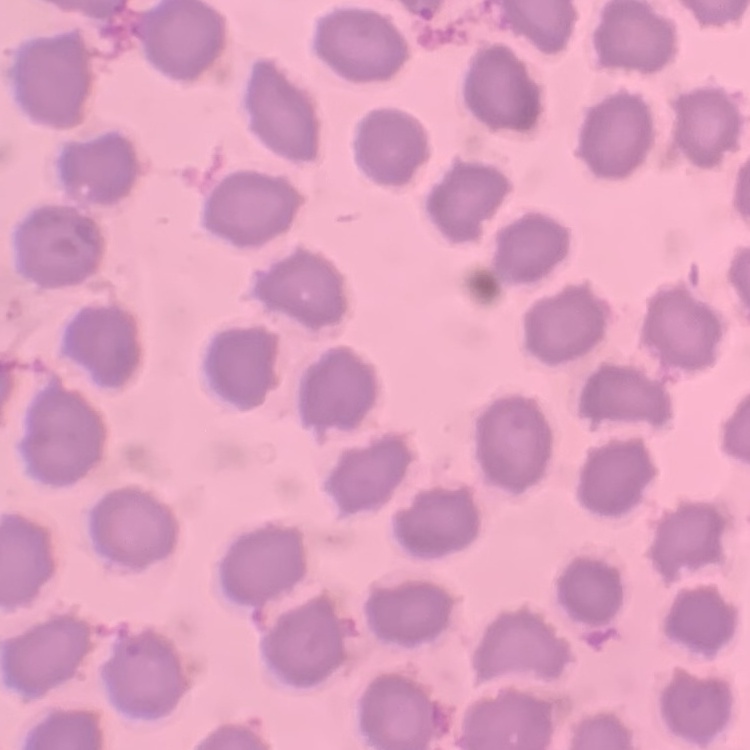
red blood cell morphology = no rouleaux formation
stain = Field's or Giemsa
image type = square crop of a larger photomicrograph
preparation = thin blood smear